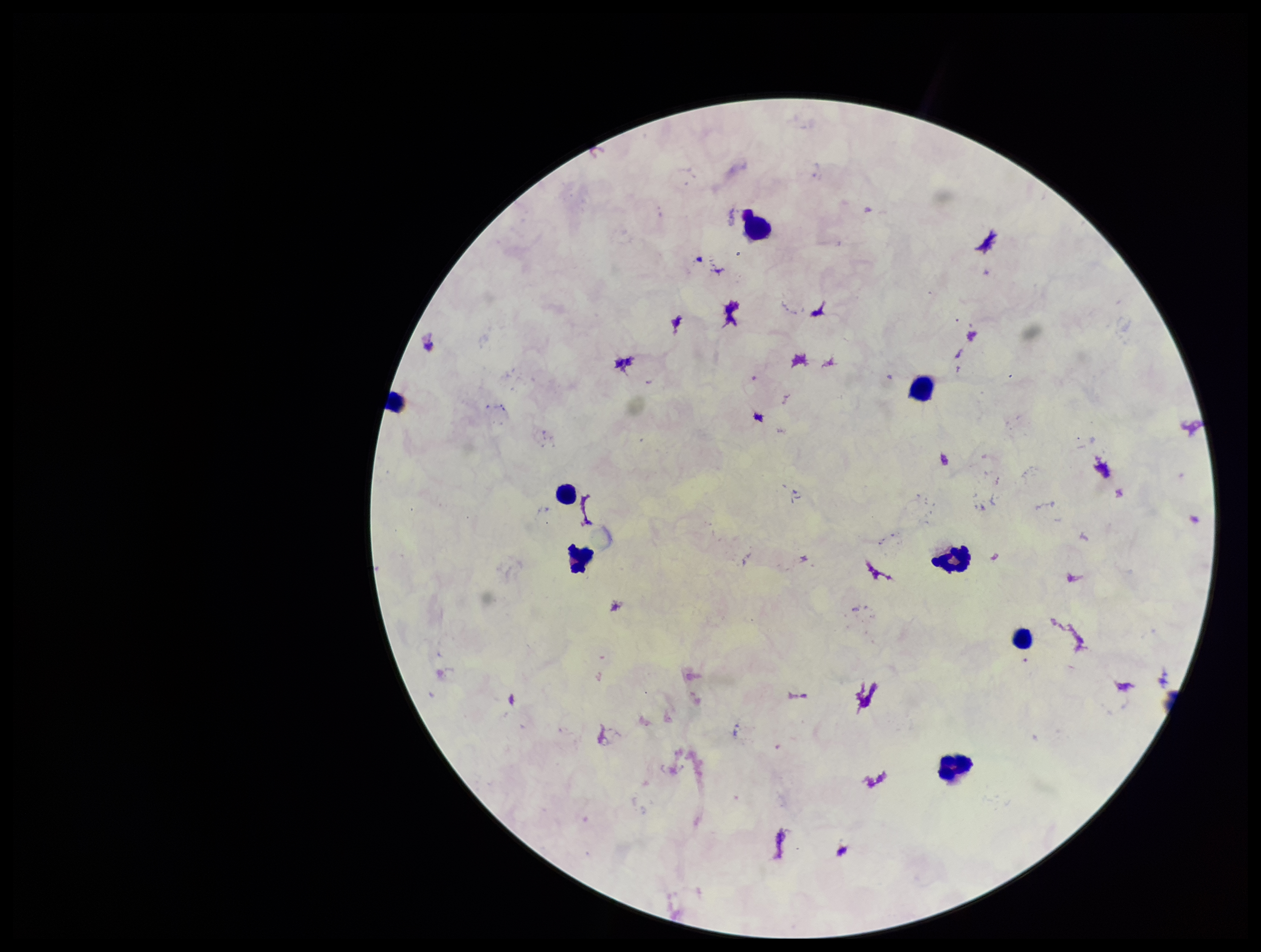 Parasite count: 0. One field from this slide. Photographed through the microscope eyepiece with a smartphone camera. Preparation: thick smear. Image is 1261×952 pixels. Plasmodium parasites: none seen. Leukocyte count: 8. Giemsa stain. Patient malaria status: negative.